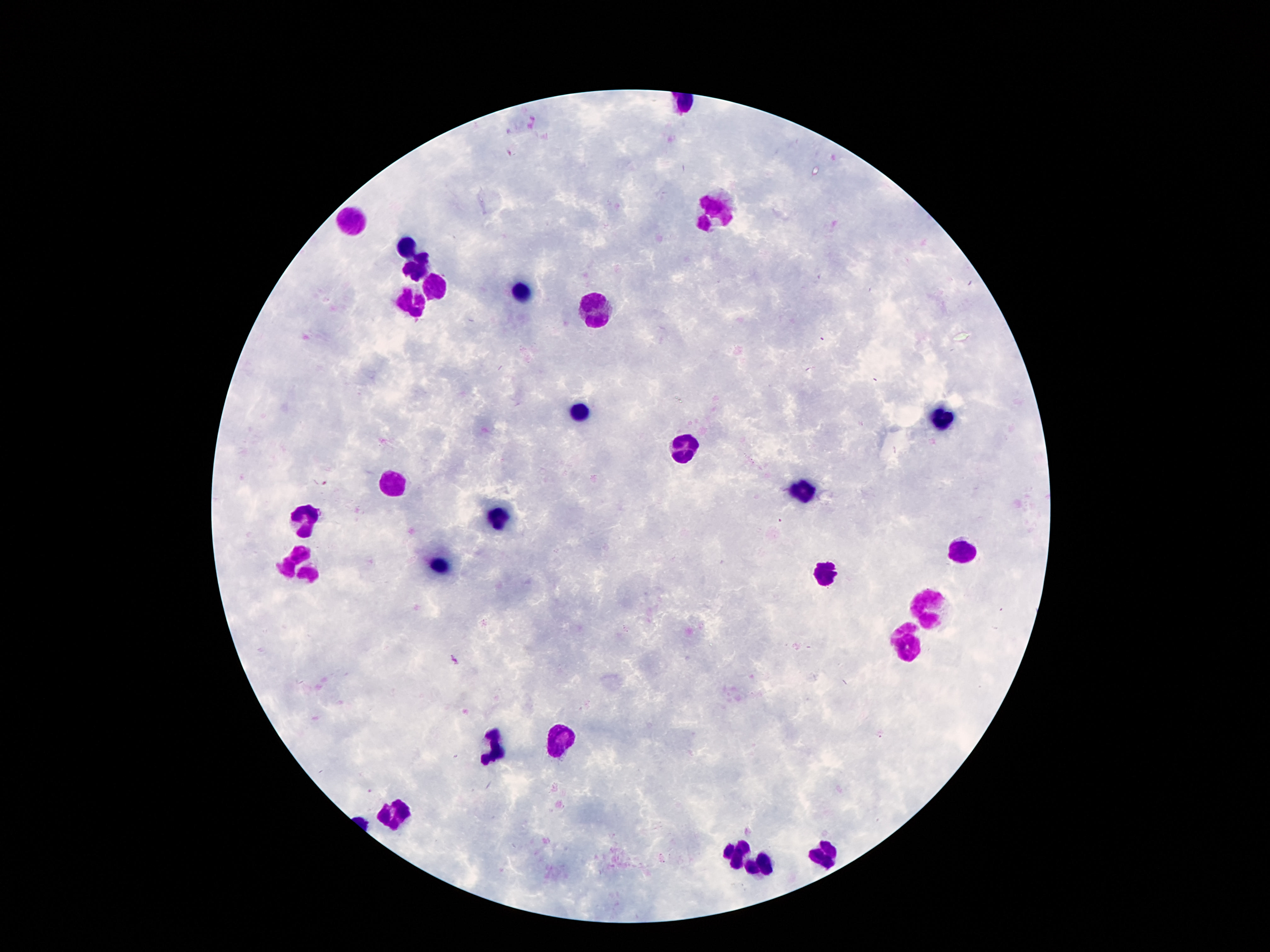

image_size: 1270×952 pixels
stain: Giemsa
field_of_view: single
preparation: thick peripheral-blood smear
leukocyte_locations: 'approximate centers as (x, y) in pixels: (717, 211), (353, 221), (405, 247), (415, 267), (431, 285), (521, 293), (407, 307), (593, 315), (579, 409), (939, 417), (685, 445), (395, 481), (803, 489), (503, 515), (309, 516), (963, 550), (437, 565), (299, 568), (825, 573), (931, 609), (909, 644), (563, 740), (497, 742), (395, 814), (737, 850), (823, 854), (763, 868)'
patient_malaria_status: uninfected
magnification: 100x
capture: smartphone camera through the microscope eyepiece